Name the cell type shown.
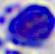

This is a leukocyte.

Micrograph. 400x magnification.